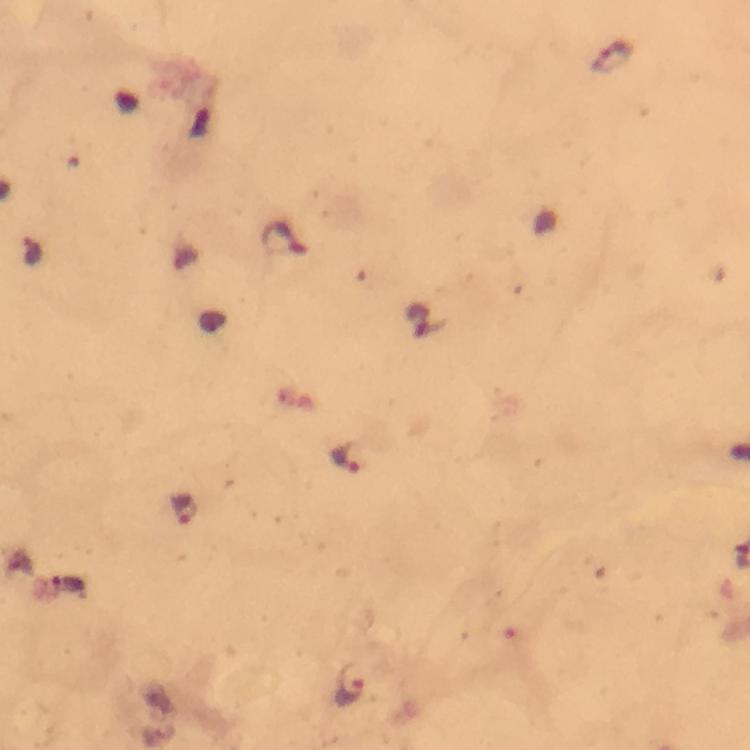

Approximate centers as [x, y] in pixels.
Summary:
  - Plasmodium parasite locations: [613, 57], [284, 240], [347, 458], [184, 512], [350, 685]
  - Immersion oil: applied
  - Image size: 750×750 pixels
  - Stain: Giemsa
  - Preparation: thick smear
  - Cropped from: one field of view
  - Capture: smartphone camera through the microscope
  - Magnification: 100x
  - Context: from a diagnostic examination for malaria